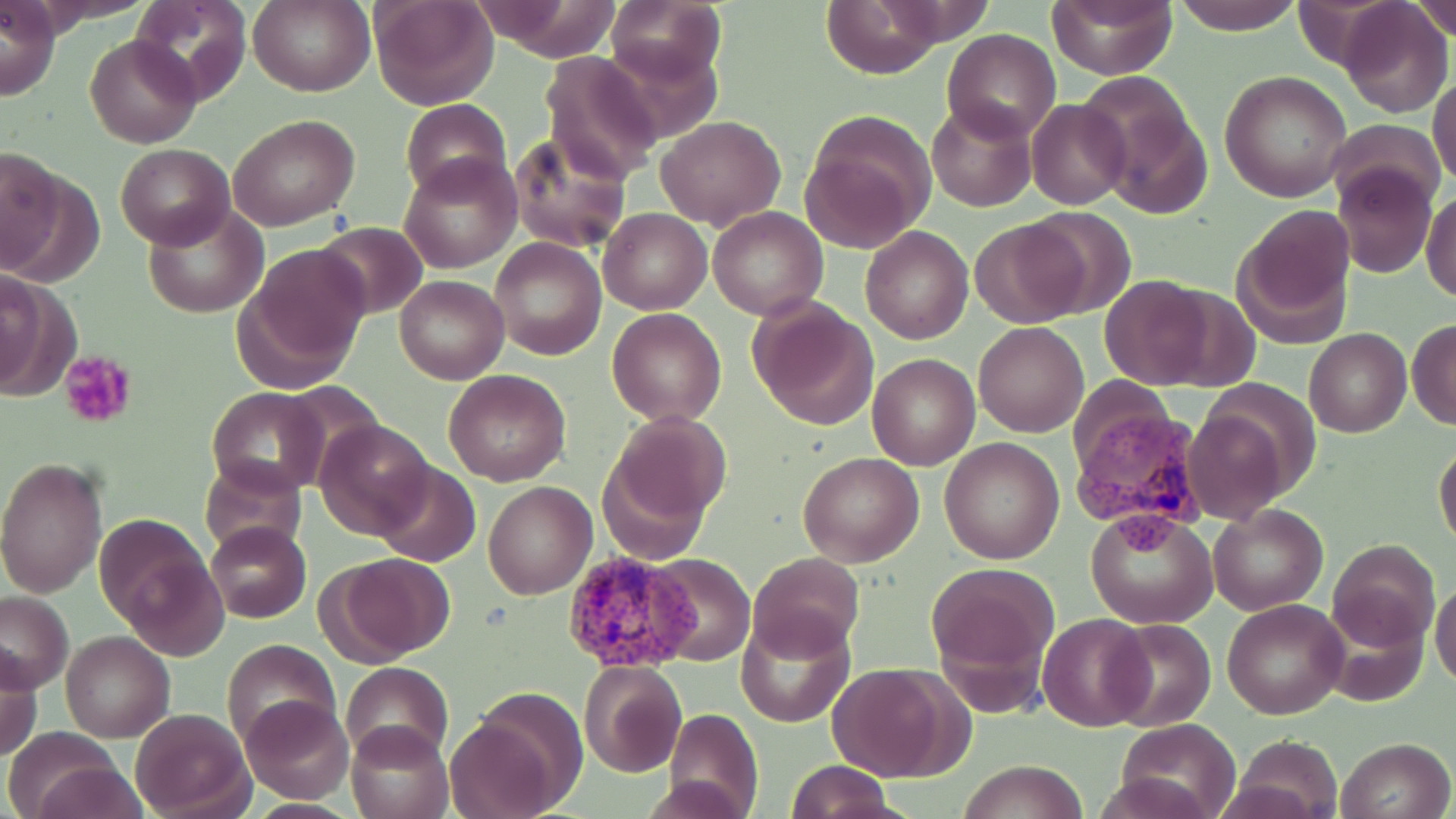
Summary:
  - Coordinate format: approximate bounding boxes as (x1, y1, x2, y2) in pixels
  - Plasmodium vivax-infected red blood cell locations: (1071, 399, 1208, 554), (564, 549, 698, 675)
  - Uninfected red blood cell locations: (128, 0, 252, 106), (250, 0, 374, 97), (370, 0, 498, 110), (469, 0, 625, 63), (1047, 0, 1180, 79), (1171, 0, 1307, 35), (606, 1, 728, 91), (818, 1, 949, 78), (1338, 1, 1452, 119), (1403, 1, 1456, 42), (1, 2, 61, 101), (943, 29, 1061, 145), (85, 34, 201, 149), (539, 51, 663, 185), (1220, 70, 1352, 202), (1429, 74, 1456, 189), (1081, 76, 1212, 216), (1025, 97, 1131, 210), (400, 98, 513, 203), (927, 102, 1036, 211), (799, 112, 936, 251), (227, 113, 361, 230), (655, 115, 786, 230), (1327, 118, 1447, 210), (507, 132, 631, 255), (116, 144, 233, 249), (1, 151, 89, 281), (400, 154, 520, 275), (1332, 162, 1438, 279), (1422, 189, 1455, 305), (143, 204, 268, 319), (707, 206, 829, 320), (598, 207, 710, 314), (1022, 208, 1136, 317), (1233, 209, 1356, 344), (968, 218, 1091, 328), (316, 221, 429, 320), (860, 226, 973, 344), (490, 238, 606, 360), (233, 243, 373, 391), (0, 266, 77, 400), (394, 275, 508, 384), (1099, 276, 1216, 390), (747, 296, 877, 431), (606, 309, 725, 427), (1407, 319, 1456, 430), (973, 320, 1089, 437), (1304, 327, 1411, 438), (868, 353, 980, 470), (442, 368, 571, 485), (208, 386, 327, 495), (1185, 397, 1300, 524), (605, 410, 730, 528), (314, 419, 436, 540), (939, 437, 1065, 564), (1434, 441, 1456, 553), (597, 451, 710, 567), (797, 452, 923, 567), (196, 455, 308, 559), (0, 456, 108, 599), (372, 463, 480, 566), (484, 482, 596, 598), (1208, 502, 1329, 615), (1086, 508, 1217, 629), (98, 514, 225, 653), (206, 521, 311, 623), (1329, 540, 1439, 648), (747, 551, 866, 661), (326, 552, 456, 663), (646, 554, 755, 667), (926, 562, 1058, 696), (1430, 582, 1456, 690), (0, 592, 74, 691), (1222, 600, 1347, 720), (736, 613, 853, 728), (1038, 613, 1154, 731), (1103, 619, 1217, 730), (61, 632, 173, 742), (221, 638, 341, 750), (1, 649, 44, 762), (580, 660, 685, 778), (339, 662, 454, 763), (828, 664, 961, 781), (241, 695, 354, 804), (448, 702, 574, 819), (128, 707, 254, 817), (664, 707, 763, 819), (1115, 718, 1239, 819), (345, 721, 454, 819), (5, 726, 125, 819), (1229, 734, 1343, 819), (1335, 736, 1454, 819), (30, 759, 149, 819), (956, 759, 1091, 818), (788, 760, 893, 819)
  - Platelet locations: (58, 350, 137, 429)
  - Slide-level diagnosis: Plasmodium vivax
  - Field of view: one of a larger specimen
  - Preparation: thin blood film
  - Magnification: 1000x
  - Stain: May-Grünwald-Giemsa
  - Image size: 1456×819 pixels
  - Modality: light microscopy